Classify this cell by malaria status.
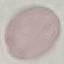
It is uninfected.

preparation = thin blood smear
capture = smartphone through the microscope eyepiece
image type = cell patch, automatically extracted from a larger field of view and resized to 64 × 64 pixels
stain = Giemsa